Assess the morphology of the erythrocytes.
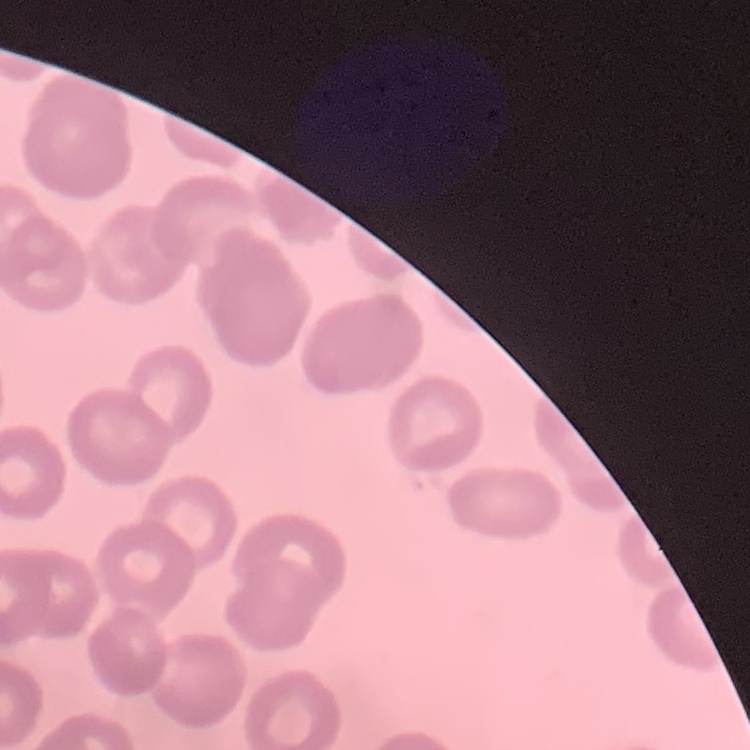
No rouleaux formation.

Summary:
  - Preparation: thin blood smear
  - Image type: one tile cut from a larger photomicrograph
  - Stain: Field's or Giemsa